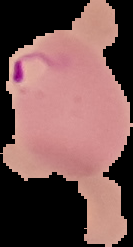

preparation = thin blood smear
result = malaria parasites detected
image size = 133×247 pixels
image type = segmented cell region on a black background